Point out each Plasmodium parasite.
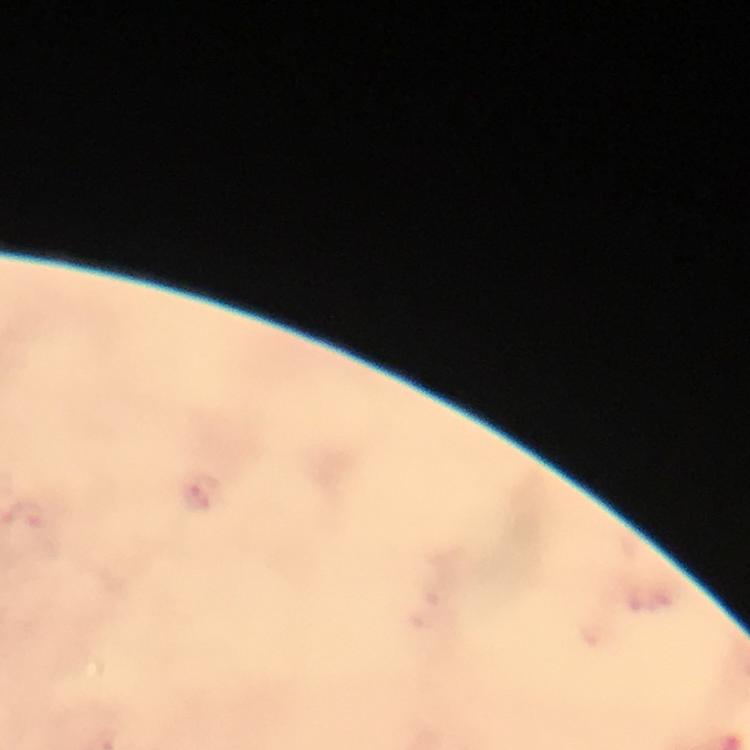

Approximate centers as {x, y} in pixels.
Plasmodium parasites: {199, 496}.

Summary:
  - Immersion oil: used
  - Magnification: 100x
  - Cropped from: one field of view
  - Stain: Giemsa
  - Capture: smartphone mounted on the microscope
  - Preparation: thick blood film
  - Context: from a malaria diagnostic workup
  - Image size: 750×750 pixels